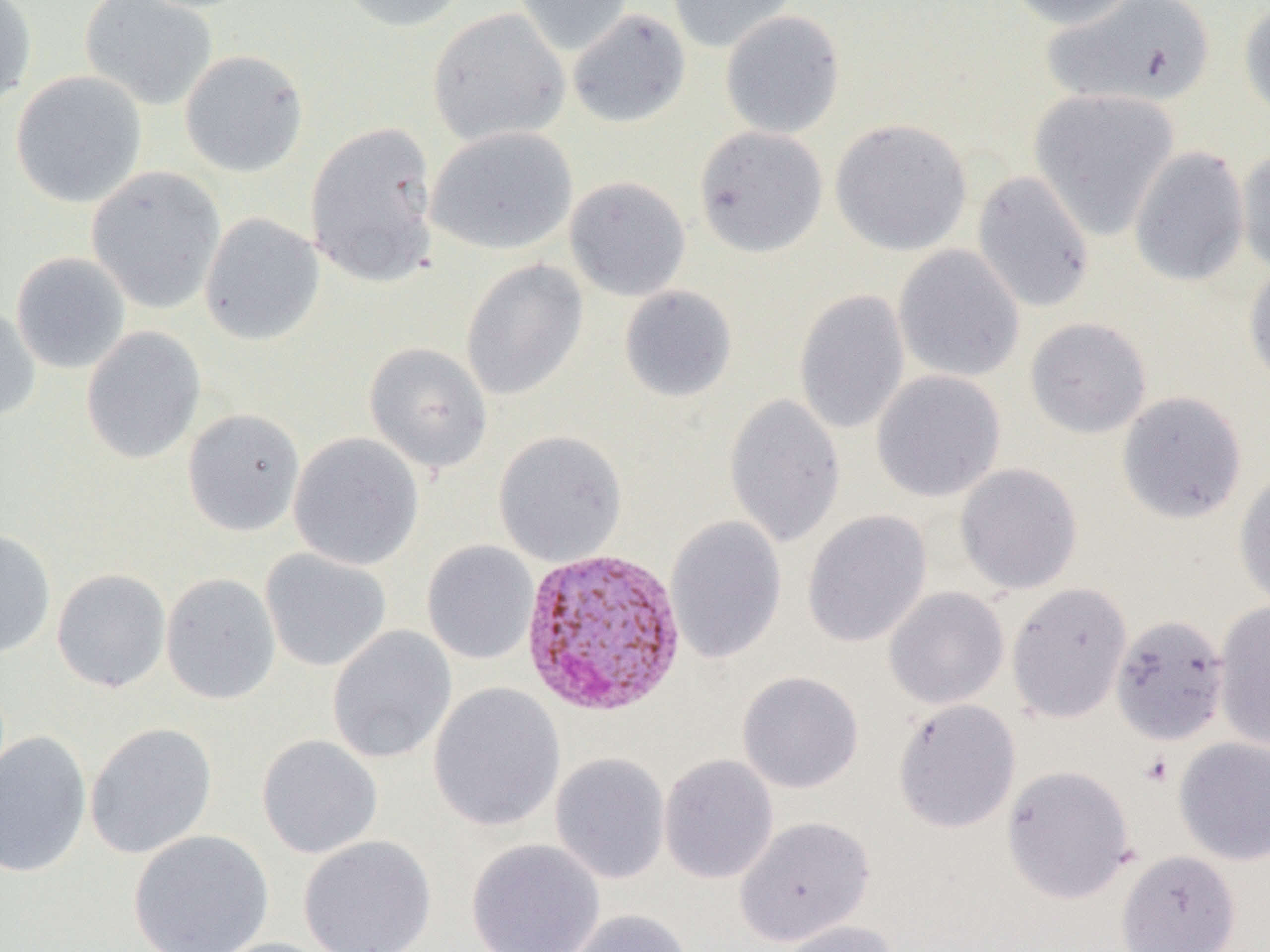
slide-level diagnosis = Plasmodium vivax
magnification = 1000x
image size = 1270×952 pixels
field of view = one of a larger specimen
preparation = thin blood smear
Plasmodium vivax-infected red blood cell locations = approximate bounding boxes as named x1/y1/x2/y2 corners in pixels: (x1=520, y1=545, x2=688, y2=720)
platelet locations = approximate bounding boxes as named x1/y1/x2/y2 corners in pixels: (x1=1139, y1=753, x2=1174, y2=787)
modality = optical microscopy
uninfected red blood cell locations = approximate bounding boxes as named x1/y1/x2/y2 corners in pixels: (x1=0, y1=0, x2=37, y2=111), (x1=79, y1=0, x2=218, y2=111), (x1=337, y1=0, x2=472, y2=33), (x1=513, y1=0, x2=634, y2=56), (x1=666, y1=0, x2=799, y2=54), (x1=1004, y1=0, x2=1144, y2=30), (x1=1043, y1=0, x2=1217, y2=109), (x1=1238, y1=2, x2=1270, y2=120), (x1=427, y1=7, x2=570, y2=146), (x1=567, y1=8, x2=691, y2=129), (x1=719, y1=9, x2=846, y2=139), (x1=179, y1=49, x2=309, y2=177), (x1=10, y1=71, x2=147, y2=208), (x1=1028, y1=88, x2=1180, y2=240), (x1=829, y1=118, x2=973, y2=256), (x1=305, y1=120, x2=440, y2=287), (x1=693, y1=125, x2=828, y2=258), (x1=425, y1=126, x2=578, y2=255), (x1=1129, y1=146, x2=1250, y2=288), (x1=1236, y1=149, x2=1270, y2=277), (x1=85, y1=166, x2=226, y2=314), (x1=972, y1=170, x2=1096, y2=314), (x1=564, y1=176, x2=691, y2=301), (x1=200, y1=212, x2=324, y2=346), (x1=893, y1=245, x2=1025, y2=382), (x1=11, y1=251, x2=131, y2=374), (x1=460, y1=259, x2=589, y2=401), (x1=1243, y1=261, x2=1270, y2=390), (x1=618, y1=285, x2=738, y2=403), (x1=793, y1=289, x2=910, y2=435), (x1=0, y1=304, x2=41, y2=422), (x1=1025, y1=317, x2=1152, y2=439), (x1=81, y1=326, x2=206, y2=464), (x1=364, y1=342, x2=493, y2=474), (x1=871, y1=369, x2=1006, y2=502), (x1=1116, y1=391, x2=1248, y2=524), (x1=723, y1=393, x2=845, y2=549), (x1=182, y1=408, x2=305, y2=536), (x1=493, y1=430, x2=628, y2=566), (x1=288, y1=433, x2=424, y2=571), (x1=954, y1=462, x2=1083, y2=595), (x1=1233, y1=465, x2=1270, y2=611), (x1=802, y1=510, x2=932, y2=647), (x1=665, y1=516, x2=787, y2=663), (x1=0, y1=528, x2=56, y2=659), (x1=422, y1=540, x2=539, y2=665), (x1=260, y1=548, x2=391, y2=673), (x1=51, y1=568, x2=171, y2=693), (x1=160, y1=573, x2=281, y2=704), (x1=1006, y1=582, x2=1133, y2=723), (x1=883, y1=586, x2=1010, y2=710), (x1=1213, y1=601, x2=1270, y2=751), (x1=1110, y1=612, x2=1230, y2=745), (x1=327, y1=626, x2=456, y2=764), (x1=737, y1=671, x2=864, y2=793), (x1=428, y1=682, x2=565, y2=831), (x1=893, y1=698, x2=1021, y2=833), (x1=84, y1=722, x2=217, y2=859), (x1=0, y1=731, x2=91, y2=878), (x1=256, y1=734, x2=383, y2=859), (x1=1173, y1=736, x2=1270, y2=865), (x1=550, y1=753, x2=670, y2=884), (x1=659, y1=754, x2=778, y2=884), (x1=1002, y1=764, x2=1135, y2=904), (x1=735, y1=815, x2=875, y2=945), (x1=128, y1=829, x2=273, y2=952), (x1=298, y1=835, x2=437, y2=952), (x1=466, y1=838, x2=605, y2=951), (x1=1116, y1=849, x2=1241, y2=952), (x1=564, y1=908, x2=693, y2=952), (x1=773, y1=920, x2=901, y2=952), (x1=204, y1=938, x2=341, y2=952)